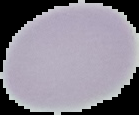
preparation = thin blood smear
result = no Plasmodium parasites seen
image type = segmented cell region on a black background
image size = 139×115 pixels